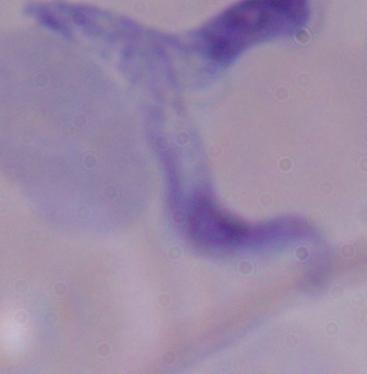 A trypanosome is seen. Captured at 1000x magnification. Micrograph.